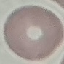

malaria status = uninfected
image type = automatically extracted cell patch, resized to 64 × 64 pixels
preparation = thin blood smear
stain = Giemsa
capture = smartphone through the microscope eyepiece